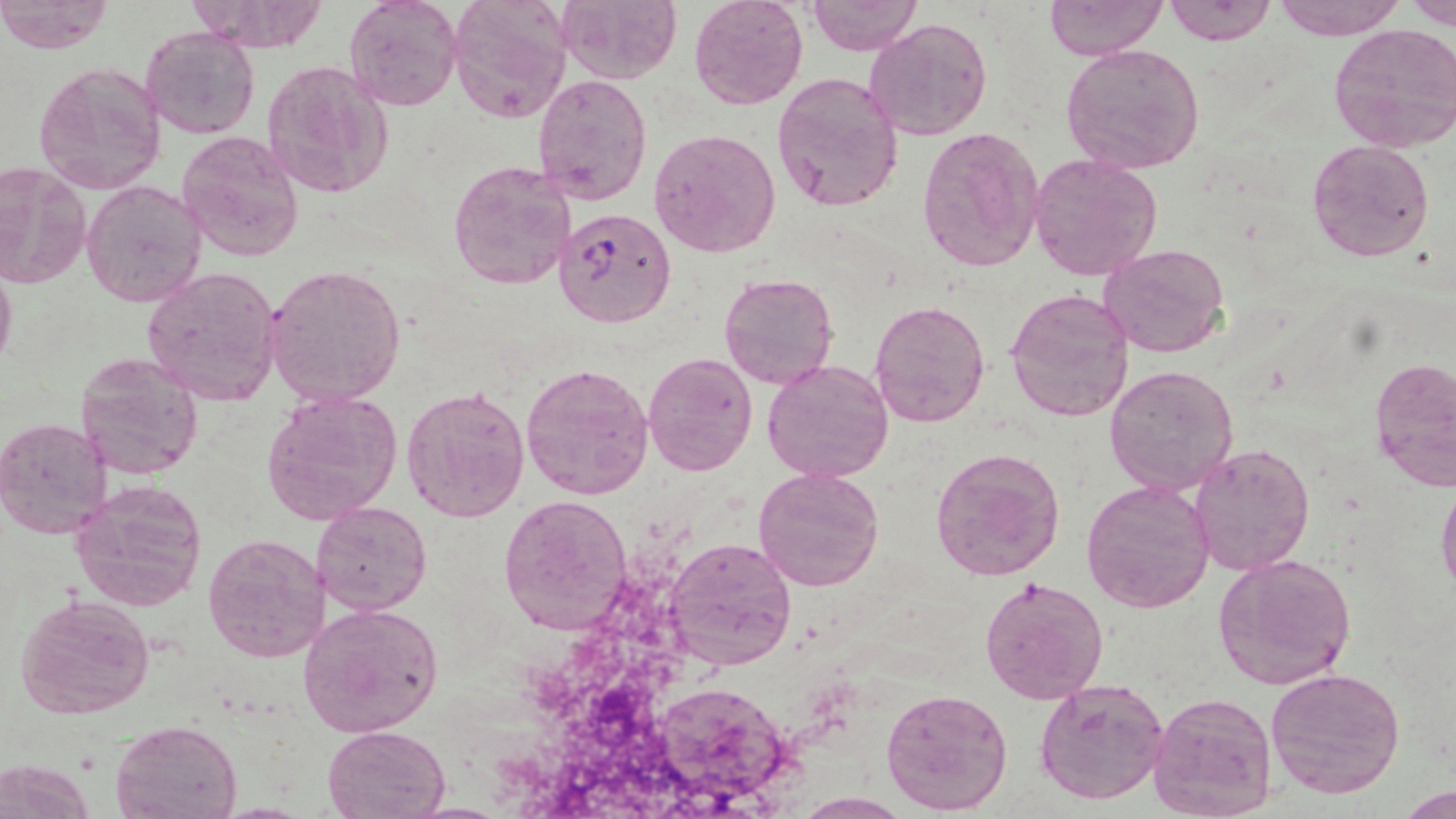
Approximate bounding boxes as (x1, y1, x2, y2) in pixels. Plasmodium falciparum-infected red blood cell locations: (553, 207, 674, 328). Uninfected red blood cell locations: (345, 0, 462, 112), (446, 0, 572, 123), (556, 0, 681, 83), (689, 0, 810, 111), (805, 0, 924, 54), (1043, 0, 1166, 61), (1163, 0, 1276, 46), (1271, 0, 1404, 41), (0, 1, 113, 54), (189, 1, 330, 53), (1402, 1, 1456, 26), (865, 17, 992, 141), (1327, 22, 1456, 153), (140, 25, 259, 138), (1060, 41, 1207, 176), (32, 60, 168, 194), (260, 60, 394, 199), (531, 73, 653, 206), (772, 73, 904, 214), (648, 128, 781, 258), (916, 128, 1044, 272), (177, 130, 304, 262), (1307, 140, 1434, 260), (1029, 153, 1164, 283), (447, 156, 578, 292), (0, 162, 92, 294), (82, 181, 206, 307), (1097, 243, 1232, 357), (0, 258, 17, 379), (263, 262, 408, 406), (140, 265, 282, 406), (720, 272, 838, 390), (1005, 288, 1135, 422), (869, 299, 992, 429), (644, 352, 757, 475), (73, 353, 203, 479), (1370, 354, 1455, 493), (762, 358, 894, 483), (521, 363, 656, 499), (1104, 365, 1241, 498), (401, 386, 530, 521), (262, 389, 403, 523), (0, 416, 113, 539), (1189, 442, 1314, 575), (930, 447, 1065, 581), (753, 465, 885, 592), (1082, 478, 1216, 614), (69, 479, 209, 612), (1437, 480, 1456, 599), (498, 493, 633, 636), (312, 502, 433, 615), (202, 533, 331, 662), (665, 534, 797, 669), (1213, 554, 1358, 689), (979, 575, 1108, 704), (16, 595, 155, 719), (298, 602, 444, 738), (1265, 667, 1405, 799), (1035, 677, 1170, 805), (880, 684, 1014, 816), (656, 688, 794, 803), (1147, 691, 1279, 818), (112, 717, 242, 818), (323, 724, 448, 818), (1, 758, 95, 818), (1400, 786, 1453, 817). Slide-level diagnosis: Plasmodium falciparum. Optical microscopy. Image is 1456×819 pixels. One field of a larger specimen. Thin blood smear. May-Grünwald-Giemsa stain. 1000x magnification.